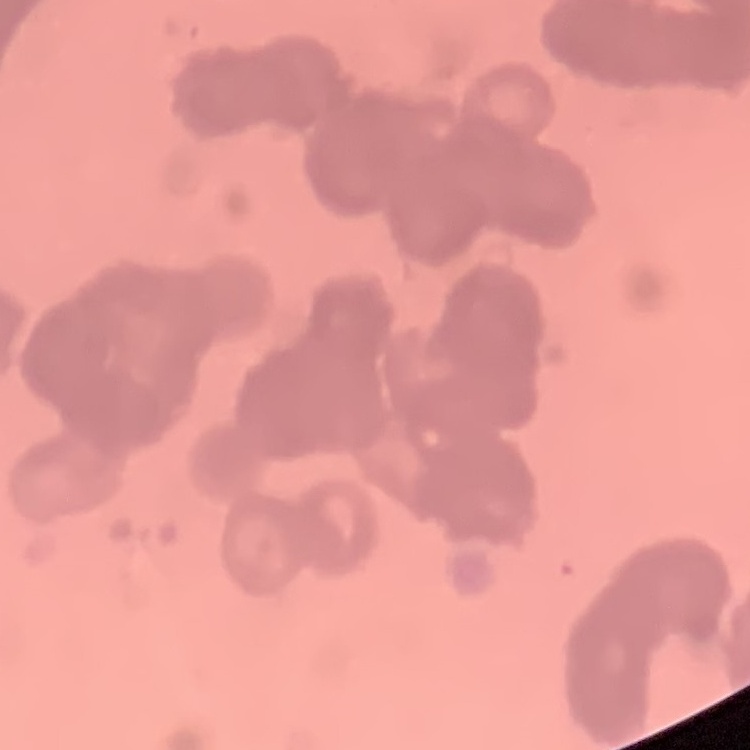
The red blood cells show rouleaux formation. One tile cut from a larger photomicrograph. Thin peripheral smear. Field's or Giemsa stain.